Identify the preparation type.
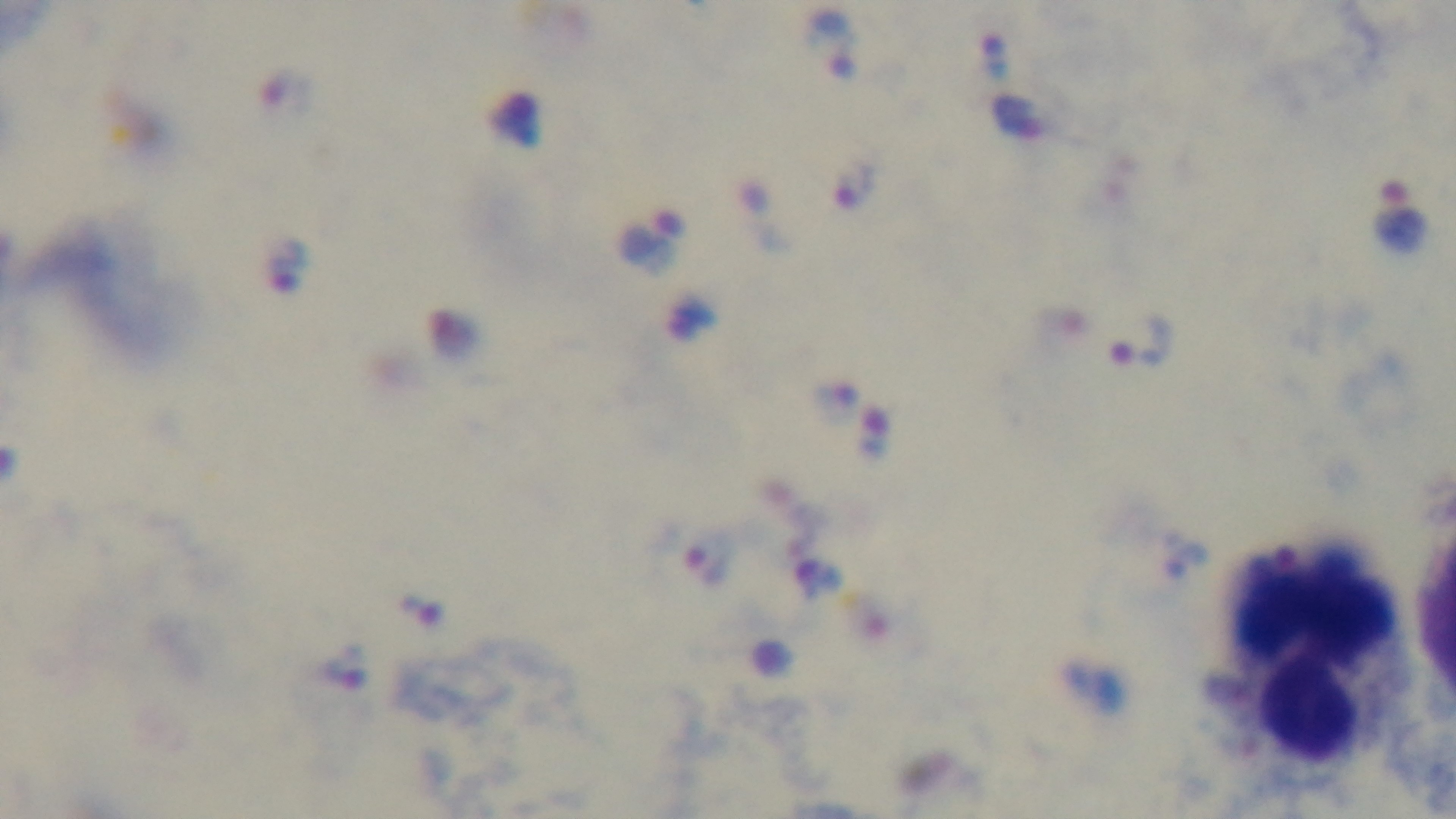

A thick smear.

Summary:
  - Stain: Giemsa
  - Malaria status: infected
  - Objective: 100x oil immersion
  - Field of view: one from the slide
  - Capture: mounted 4K digital camera
  - Modality: light microscopy